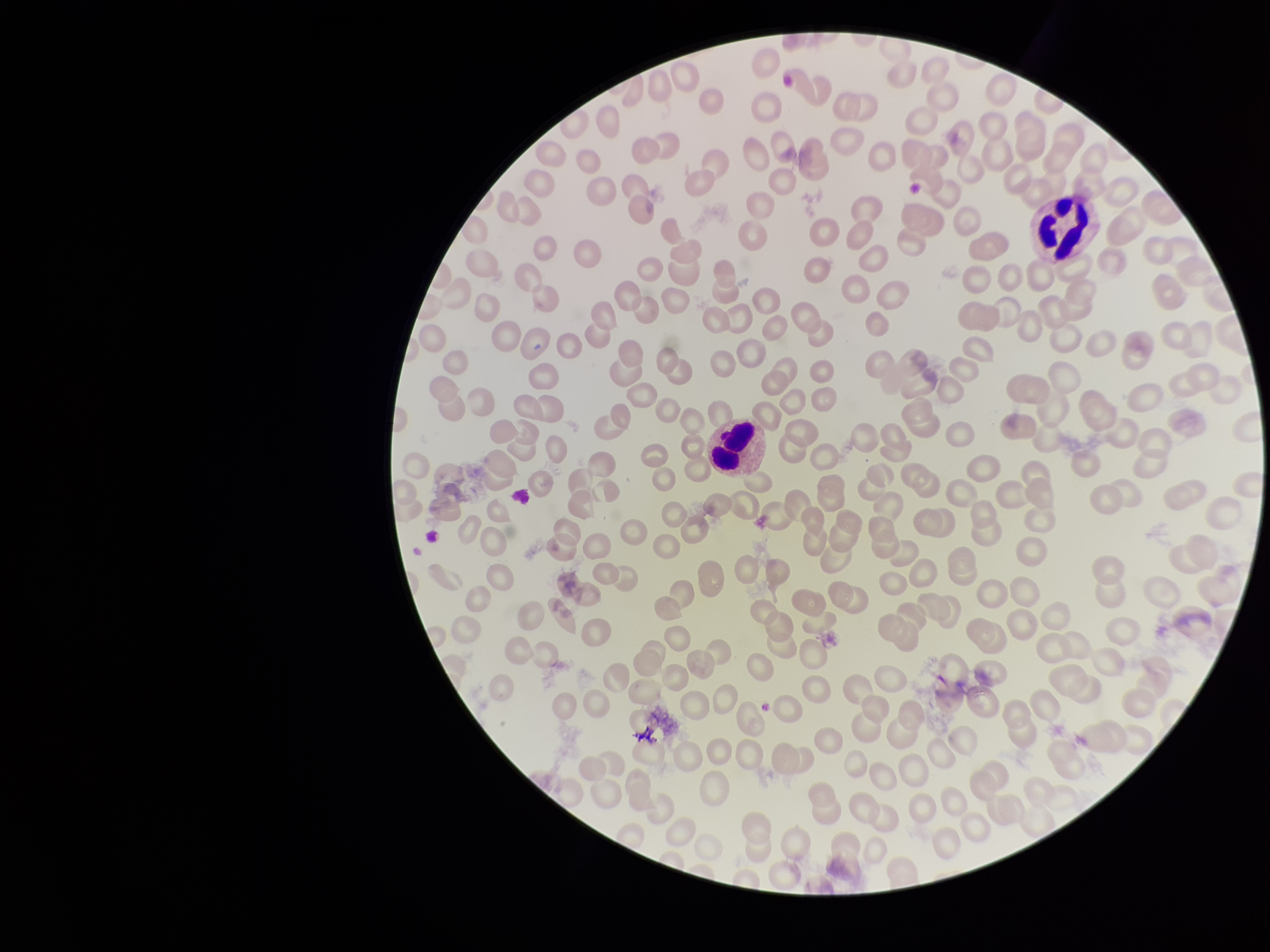
Red blood cell count: 204. Preparation: thin. Giemsa stain. Patient malaria status: negative. Parasitized red blood cells: none seen. Parasitized red blood cell count: 0. Single field of view. Photographed through the microscope eyepiece with a smartphone camera. Image is 1270×952 pixels.